Locate every blood parasite and identify its species.
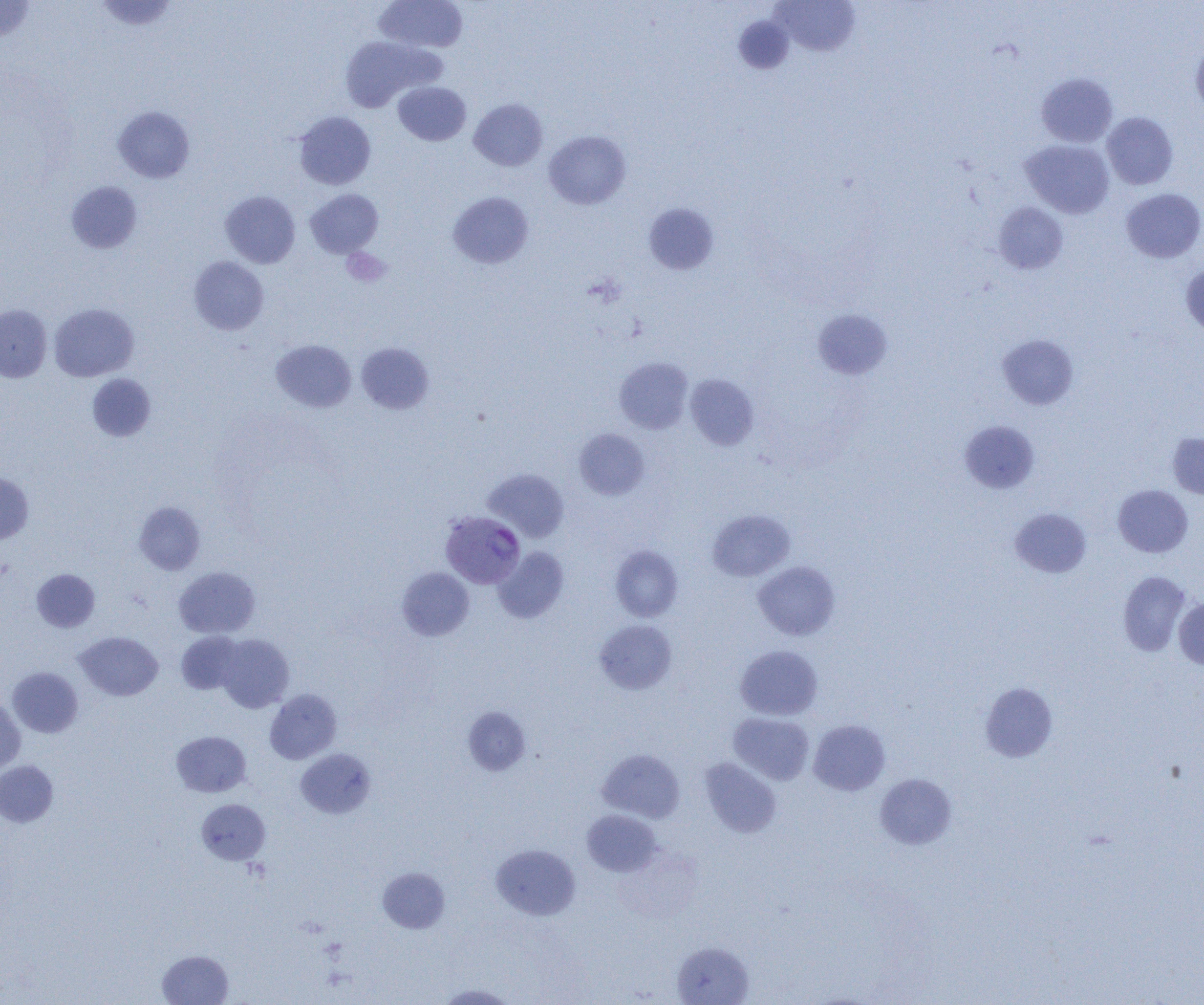

Approximate bounding boxes as named x1/y1/x2/y2 corners in pixels.
Plasmodium vivax-infected red blood cells: (x1=440, y1=511, x2=525, y2=588).
No Plasmodium falciparum, Plasmodium ovale, Plasmodium malariae, Babesia divergens, or Trypanosoma brucei observed.

Summary:
  - Uninfected red blood cell locations: (x1=0, y1=0, x2=35, y2=42), (x1=93, y1=0, x2=179, y2=32), (x1=374, y1=0, x2=468, y2=53), (x1=773, y1=1, x2=859, y2=56), (x1=733, y1=16, x2=794, y2=74), (x1=339, y1=36, x2=440, y2=111), (x1=1191, y1=39, x2=1204, y2=117), (x1=1037, y1=73, x2=1118, y2=147), (x1=393, y1=81, x2=471, y2=146), (x1=469, y1=98, x2=548, y2=171), (x1=113, y1=106, x2=195, y2=183), (x1=293, y1=111, x2=376, y2=189), (x1=1102, y1=112, x2=1178, y2=189), (x1=544, y1=131, x2=631, y2=210), (x1=1020, y1=140, x2=1115, y2=218), (x1=66, y1=181, x2=142, y2=253), (x1=1121, y1=188, x2=1204, y2=263), (x1=305, y1=189, x2=383, y2=258), (x1=221, y1=191, x2=300, y2=268), (x1=448, y1=191, x2=533, y2=268), (x1=993, y1=202, x2=1068, y2=274), (x1=643, y1=203, x2=720, y2=273), (x1=189, y1=256, x2=269, y2=334), (x1=1181, y1=264, x2=1204, y2=337), (x1=49, y1=303, x2=138, y2=382), (x1=0, y1=305, x2=52, y2=383), (x1=813, y1=308, x2=893, y2=380), (x1=997, y1=334, x2=1080, y2=409), (x1=270, y1=340, x2=356, y2=413), (x1=356, y1=342, x2=434, y2=414), (x1=614, y1=357, x2=693, y2=434), (x1=87, y1=374, x2=156, y2=442), (x1=685, y1=374, x2=759, y2=450), (x1=960, y1=421, x2=1039, y2=493), (x1=574, y1=429, x2=649, y2=500), (x1=1167, y1=433, x2=1204, y2=498), (x1=483, y1=468, x2=569, y2=542), (x1=0, y1=471, x2=33, y2=544), (x1=1113, y1=484, x2=1193, y2=558), (x1=134, y1=501, x2=206, y2=574), (x1=1010, y1=508, x2=1091, y2=578), (x1=707, y1=509, x2=795, y2=581), (x1=610, y1=546, x2=683, y2=621), (x1=493, y1=547, x2=569, y2=623), (x1=752, y1=561, x2=841, y2=640), (x1=174, y1=566, x2=260, y2=638), (x1=397, y1=567, x2=474, y2=641), (x1=31, y1=568, x2=100, y2=632), (x1=1118, y1=570, x2=1191, y2=656), (x1=1174, y1=597, x2=1204, y2=669), (x1=595, y1=620, x2=677, y2=694), (x1=176, y1=631, x2=244, y2=694), (x1=75, y1=632, x2=163, y2=700), (x1=216, y1=634, x2=294, y2=713), (x1=735, y1=645, x2=823, y2=720), (x1=7, y1=667, x2=83, y2=737), (x1=980, y1=681, x2=1057, y2=762), (x1=265, y1=689, x2=341, y2=764), (x1=0, y1=697, x2=25, y2=773), (x1=463, y1=706, x2=531, y2=774), (x1=728, y1=712, x2=814, y2=785), (x1=809, y1=719, x2=890, y2=795), (x1=171, y1=731, x2=251, y2=797), (x1=296, y1=749, x2=375, y2=818), (x1=597, y1=749, x2=685, y2=822), (x1=700, y1=758, x2=782, y2=837), (x1=0, y1=760, x2=58, y2=827), (x1=875, y1=773, x2=956, y2=849), (x1=197, y1=799, x2=270, y2=865), (x1=582, y1=810, x2=661, y2=876), (x1=491, y1=844, x2=580, y2=920), (x1=378, y1=867, x2=450, y2=932), (x1=672, y1=941, x2=754, y2=1005), (x1=157, y1=950, x2=233, y2=1005), (x1=436, y1=983, x2=517, y2=1004)
  - Platelet locations: (x1=341, y1=248, x2=391, y2=287)
  - Slide-level diagnosis: Plasmodium vivax
  - Modality: optical microscopy
  - Field of view: single
  - Image size: 1204×1005 pixels
  - Preparation: thin blood smear
  - Magnification: 1000x